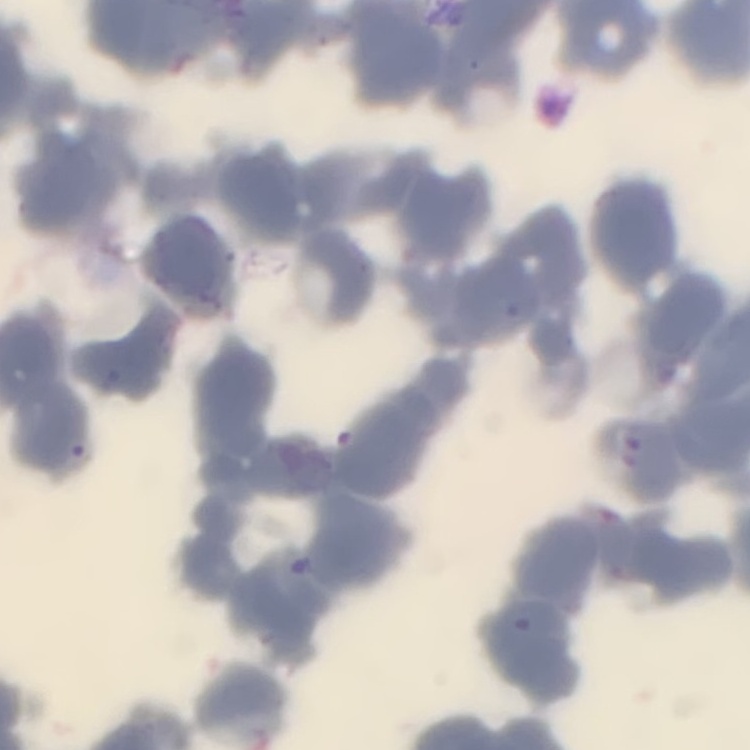

red blood cell morphology = rouleaux formation
preparation = thin peripheral smear
stain = Field's or Giemsa
image type = one tile cut from a larger photomicrograph